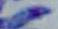

Summary:
  - Identification: Toxoplasma gondii
  - Magnification: 1000x
  - Modality: photomicrograph